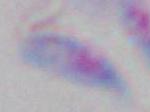

magnification: 1000x
modality: micrograph
identification: Toxoplasma gondii